Find the red blood cells that are infected with P. falciparum, and any of indeterminate infection status.
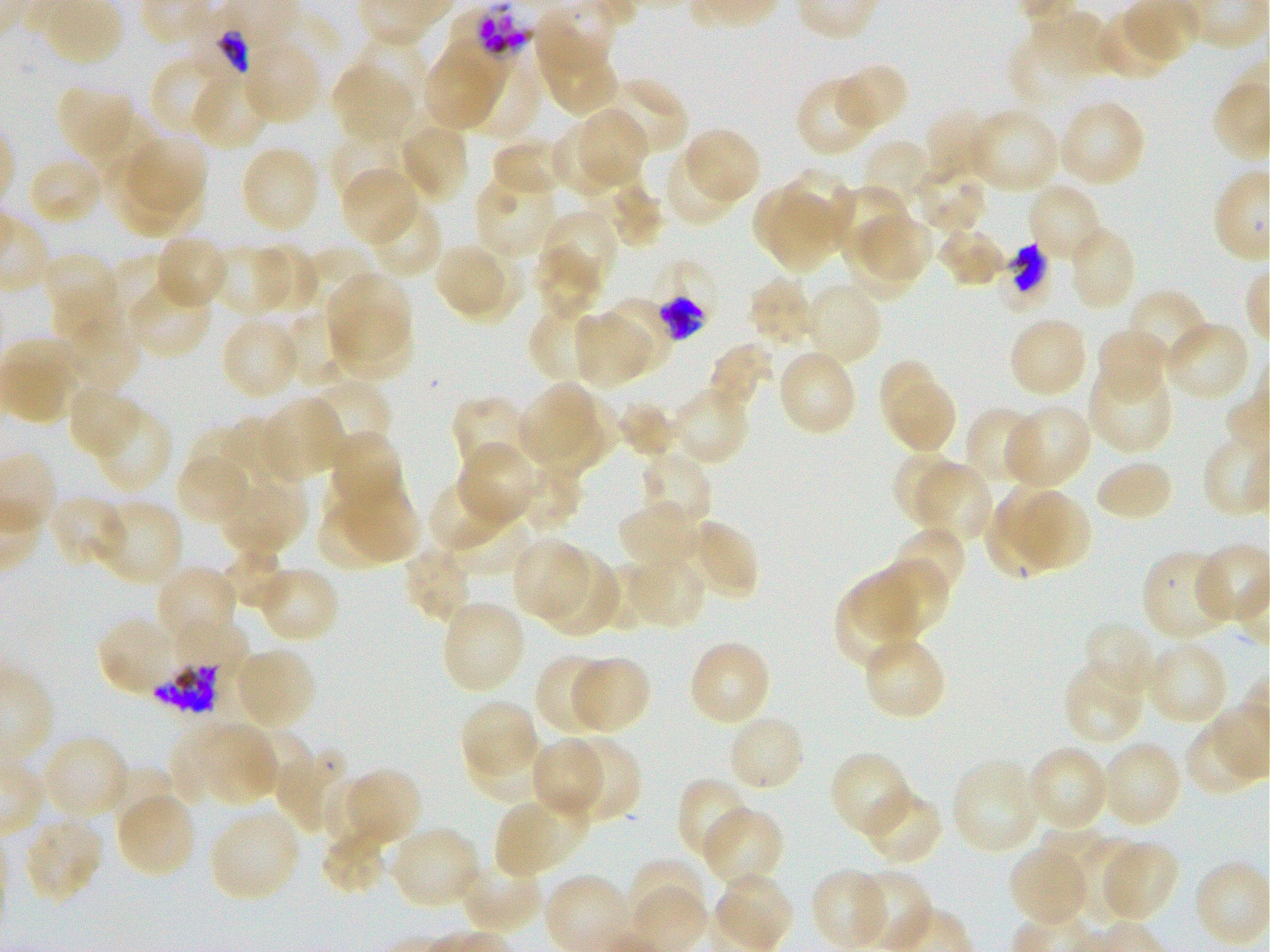
Approximate bounding boxes as [x1, y1, x2, y2] in pixels. Not every red blood cell is marked. A life-cycle stage — or a range of stages, where the recorded stages span more than one — follows each staged infected red blood cell.
Infected red blood cells: [188, 4, 264, 76] early trophozoite to early schizont; [650, 260, 715, 337] early trophozoite to early schizont; [150, 662, 221, 714].
Red blood cells of indeterminate infection status: [450, 2, 532, 78], [997, 243, 1049, 315].

Locations of uninfected red blood cells: [533, 8, 610, 73], [1095, 10, 1176, 80], [1031, 11, 1112, 79], [1011, 23, 1090, 106], [349, 36, 428, 108], [436, 37, 507, 115], [540, 37, 617, 117], [243, 41, 322, 123], [423, 49, 499, 130], [152, 52, 236, 136], [837, 63, 910, 132], [465, 64, 540, 142], [332, 67, 413, 142], [192, 71, 268, 151], [602, 75, 688, 157], [795, 77, 877, 157], [56, 84, 135, 163], [1059, 99, 1146, 188], [967, 107, 1060, 194], [924, 108, 994, 181], [574, 110, 645, 189], [399, 122, 470, 203], [549, 124, 621, 197], [682, 127, 761, 204], [328, 133, 401, 205], [129, 135, 207, 214], [490, 137, 563, 197], [860, 138, 930, 209], [240, 145, 319, 233], [663, 152, 737, 227], [26, 156, 104, 226], [586, 157, 641, 216], [106, 159, 189, 236], [907, 162, 988, 234], [782, 167, 853, 246], [341, 169, 418, 243], [474, 174, 556, 257], [1026, 181, 1103, 263], [607, 182, 667, 250], [832, 183, 908, 261], [753, 189, 821, 256], [770, 191, 834, 273], [365, 200, 442, 278], [541, 208, 617, 293], [860, 215, 934, 279], [840, 224, 919, 302], [937, 226, 1007, 286], [1072, 229, 1131, 306], [154, 235, 229, 310], [212, 244, 290, 316], [255, 244, 319, 313], [433, 244, 504, 312], [309, 247, 374, 309], [533, 247, 600, 319], [40, 253, 119, 323], [108, 254, 165, 327], [450, 255, 524, 322], [327, 272, 410, 356], [747, 277, 816, 348], [126, 278, 213, 359], [805, 283, 883, 368], [55, 284, 123, 354], [1125, 287, 1210, 368], [597, 300, 669, 378], [335, 309, 413, 380], [530, 309, 601, 383], [572, 311, 649, 387], [278, 313, 356, 390], [63, 314, 139, 395], [1008, 316, 1088, 398], [220, 317, 301, 400], [1164, 320, 1251, 403], [1097, 327, 1168, 404], [708, 342, 771, 412], [777, 349, 858, 436], [881, 361, 932, 430], [1088, 365, 1175, 454], [309, 379, 392, 456], [67, 383, 140, 458], [521, 384, 594, 463], [889, 384, 957, 453], [672, 385, 751, 467], [559, 392, 622, 459], [262, 396, 343, 480], [450, 396, 528, 475], [616, 401, 677, 458], [1002, 405, 1092, 491], [94, 406, 171, 493], [963, 406, 1041, 488], [533, 412, 604, 478], [223, 419, 298, 480], [188, 427, 254, 492], [328, 432, 405, 516], [458, 441, 537, 524], [638, 451, 712, 533], [889, 452, 960, 526], [175, 454, 253, 525], [516, 461, 583, 533], [916, 462, 993, 544], [1096, 464, 1170, 519], [245, 474, 308, 546], [218, 476, 291, 554], [428, 479, 512, 555], [341, 481, 421, 562], [994, 484, 1071, 556], [1017, 490, 1089, 571], [49, 495, 128, 570], [316, 496, 392, 572], [97, 499, 183, 587], [985, 500, 1060, 579], [617, 501, 700, 573], [452, 511, 532, 574], [688, 519, 760, 601], [891, 524, 967, 599], [512, 538, 588, 621], [223, 544, 289, 607], [401, 545, 473, 623], [1141, 549, 1230, 642], [537, 553, 622, 636], [627, 555, 707, 630], [872, 559, 951, 639], [604, 562, 670, 631], [160, 565, 239, 637], [256, 565, 341, 643], [846, 570, 918, 641], [834, 579, 921, 672], [441, 599, 526, 694], [97, 614, 177, 696], [173, 616, 249, 683], [1082, 620, 1159, 700], [687, 639, 771, 727], [1146, 639, 1230, 726], [868, 640, 943, 715], [234, 647, 317, 729], [535, 654, 612, 735], [571, 656, 652, 734], [1063, 664, 1146, 746], [461, 700, 538, 777], [728, 714, 806, 794], [170, 723, 238, 803], [200, 723, 274, 803], [251, 730, 310, 793], [466, 731, 541, 801], [40, 735, 131, 820], [562, 737, 642, 822], [531, 738, 605, 821], [1101, 739, 1183, 830], [1026, 744, 1109, 832], [275, 749, 347, 834], [829, 750, 913, 838], [951, 759, 1041, 854], [343, 767, 421, 846], [110, 768, 176, 829], [679, 777, 753, 861], [323, 778, 375, 847], [861, 787, 944, 866], [116, 791, 195, 878], [493, 799, 579, 877], [702, 806, 785, 887], [209, 809, 301, 902], [24, 817, 103, 905], [389, 826, 480, 909], [1039, 828, 1103, 886], [319, 829, 390, 895], [1076, 838, 1144, 926], [1099, 838, 1178, 922], [1008, 846, 1089, 926], [629, 857, 709, 927], [457, 860, 543, 935], [809, 868, 887, 949], [852, 870, 932, 949], [715, 873, 793, 948]. Thin blood film. Giemsa-stained preparation. 100x objective under oil immersion, numerical aperture 1.25. Static in-vitro culture of P. falciparum strain 3D7. Image is 1270×952 pixels. Single field of view. Blood group of the donor: O+.